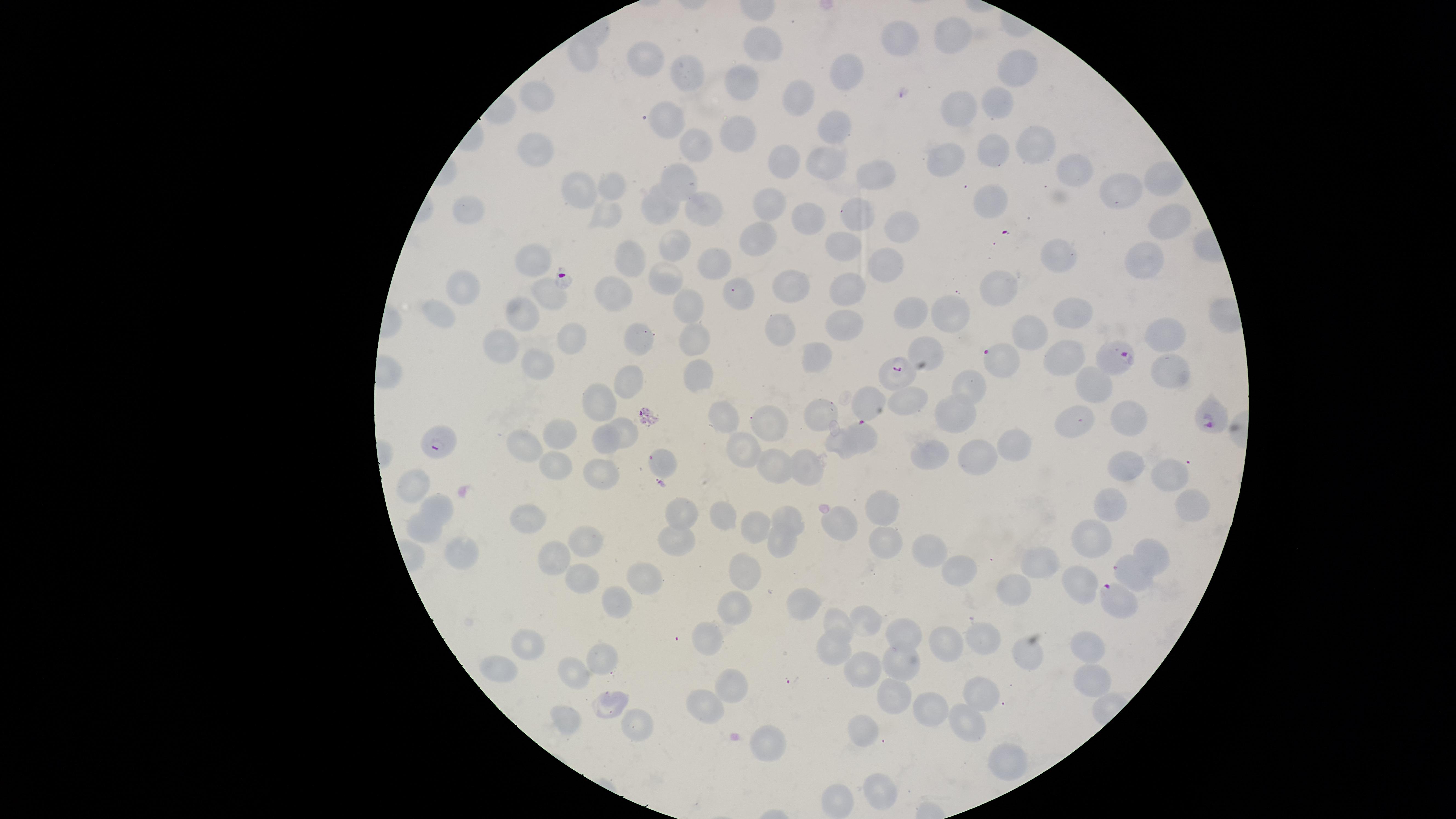

Approximate marker points as (x, y) in pixels. Parasitized RBCs: (1113, 357), (998, 360), (899, 373), (1211, 416), (859, 434), (441, 442), (1115, 594). Uninfected RBCs: (954, 32), (900, 38), (759, 51), (585, 57), (649, 60), (1017, 68), (692, 72), (850, 72), (742, 82), (803, 97), (540, 100), (996, 103), (957, 108), (663, 118), (834, 122), (734, 132), (1039, 143), (535, 144), (693, 146), (995, 149), (946, 157), (789, 158), (825, 162), (1072, 169), (878, 175), (1157, 179), (679, 181), (610, 183), (584, 192), (1120, 193), (768, 201), (992, 202), (705, 211), (667, 212), (858, 214), (467, 216), (606, 219), (812, 220), (1168, 222), (899, 227), (760, 237), (675, 242), (847, 245), (1054, 253), (625, 258), (711, 259), (882, 260), (532, 263), (1143, 265), (668, 275), (465, 286), (793, 286), (1003, 286), (612, 289), (734, 289), (853, 291), (549, 294), (688, 307), (1072, 309), (910, 311), (527, 312), (952, 314), (440, 316), (837, 320), (783, 330), (1164, 331), (1024, 337), (641, 341), (690, 341), (574, 344), (502, 349), (929, 350), (1063, 354), (817, 359), (538, 366), (1175, 369), (703, 376), (639, 382), (961, 384), (1094, 385), (907, 398), (871, 401), (598, 402), (825, 413), (957, 413), (1130, 416), (721, 417), (1079, 421), (771, 422), (624, 431), (561, 438), (601, 441), (524, 443), (1015, 443), (743, 449), (937, 455), (975, 456), (551, 465), (662, 466), (768, 466), (1129, 466), (601, 468), (808, 471), (1167, 471), (412, 478), (1190, 501), (1116, 503), (440, 504), (880, 507), (685, 511), (729, 513), (758, 518), (787, 518), (524, 519), (842, 522), (422, 529), (588, 538), (672, 538), (777, 543), (1091, 543), (880, 546), (935, 551), (457, 553), (556, 555), (1157, 555), (1043, 563), (1132, 569), (953, 572), (745, 576), (579, 579), (1014, 585), (1084, 585), (639, 586), (805, 599), (610, 601), (732, 601), (840, 618), (872, 622), (906, 634), (981, 634), (709, 636), (531, 642), (947, 644), (1089, 644), (830, 646), (1027, 650), (601, 658), (898, 662), (496, 665), (572, 670), (857, 670), (1089, 679), (727, 685), (983, 686), (887, 694), (610, 704), (704, 708), (937, 708), (565, 718), (633, 723), (966, 723), (865, 731), (767, 743), (1005, 757), (880, 791), (841, 800). Giemsa-stained preparation. Thin blood film. Image is 1456×819 pixels. Single field of view. Species: Plasmodium falciparum. Smartphone photograph through the microscope eyepiece. Circular visible region. Presence: malaria parasites seen.